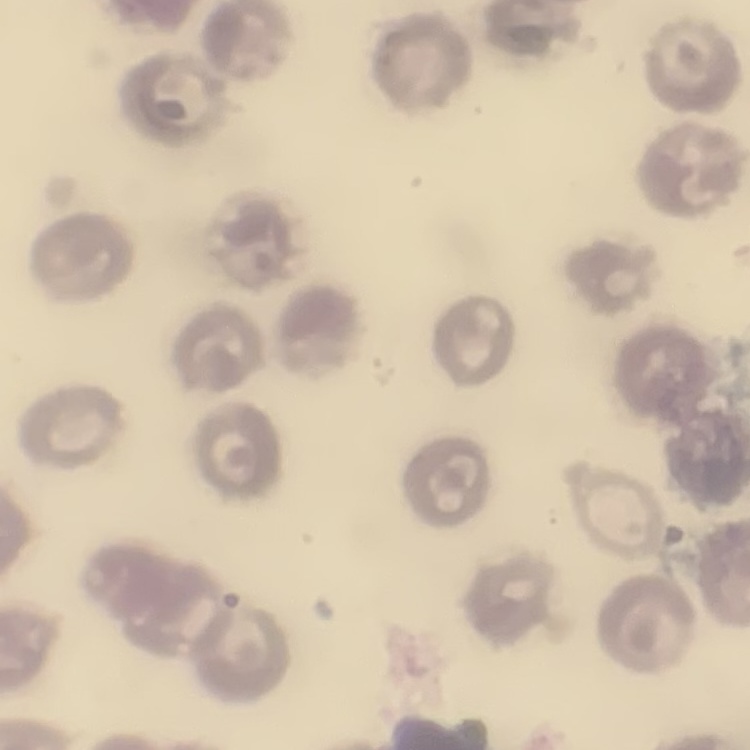
red_blood_cell_morphology: no rouleaux formation
stain: Field's or Giemsa
image_type: square crop of a larger photomicrograph
preparation: thin blood film